Give a bounding box for every parasitised red blood cell, every trophozoite, every gametocyte, every leukocyte, and every artifact (platelet-like body, stain precipitate, or debris).
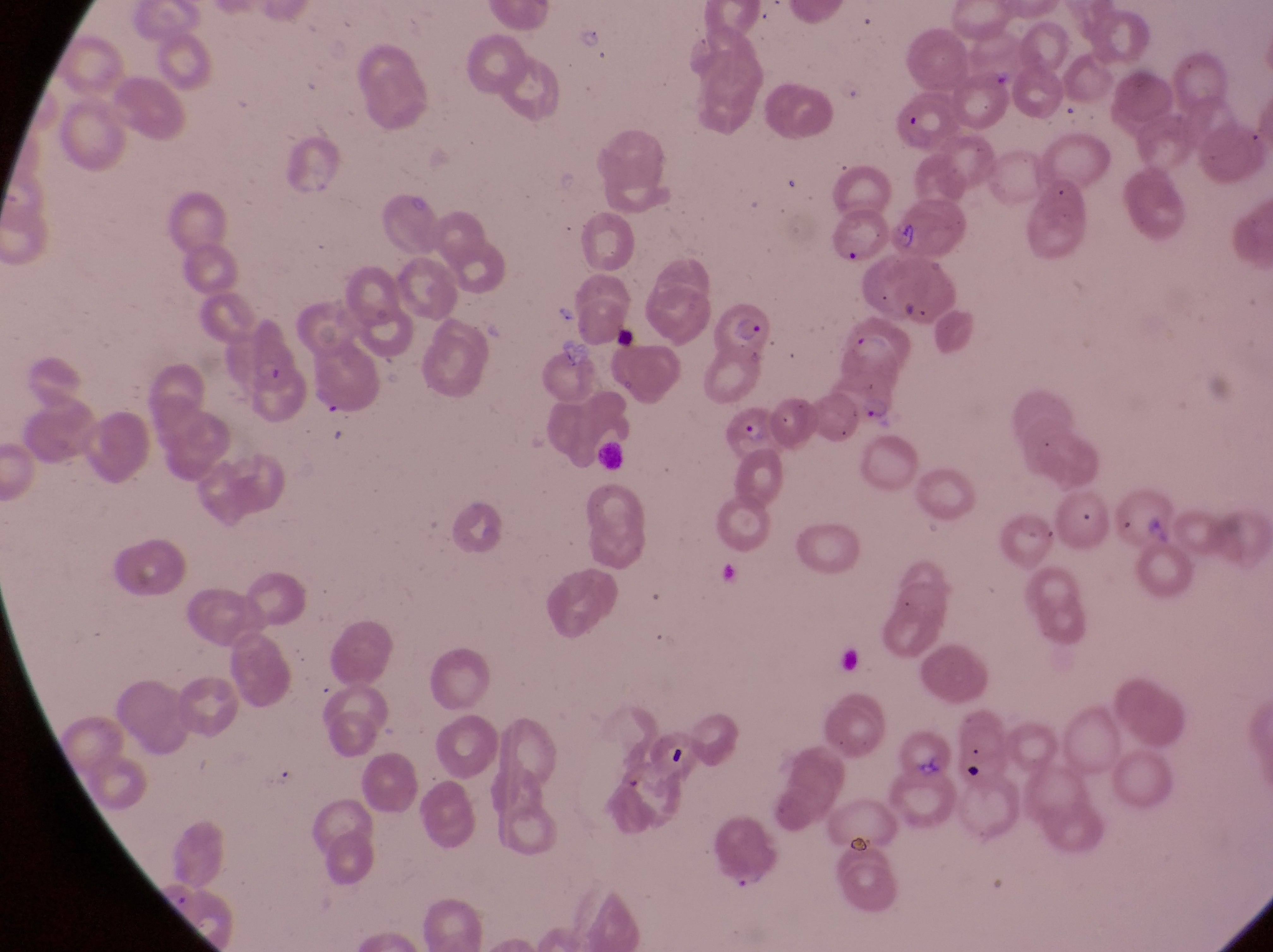
Approximate bounding boxes as {left, top, right, bottom} in pixels.
Parasitised red blood cells: {711, 302, 774, 357}, {237, 330, 302, 400}, {722, 407, 784, 464}.
Leukocytes: {599, 439, 637, 473}.
Artifacts (platelet-like body, stain precipitate, or debris): {664, 741, 694, 778}, {958, 762, 988, 785}.

magnification = 1000x
preparation = thin blood film
capture = smartphone photograph through the eyepiece of an Olympus CX-23 microscope
image size = 1273×952 pixels
field of view = single
country = Uganda